Report the malaria status of this cell.
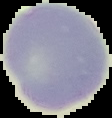
Uninfected.

Summary:
  - Image size: 112×118 pixels
  - Preparation: thin blood film
  - Image type: segmented cell region on a black background